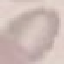
Malaria status: uninfected. Acquired by smartphone through the microscope eyepiece. Thin blood smear. Automatically extracted cell patch, resized to 64 × 64 pixels. Giemsa stain.